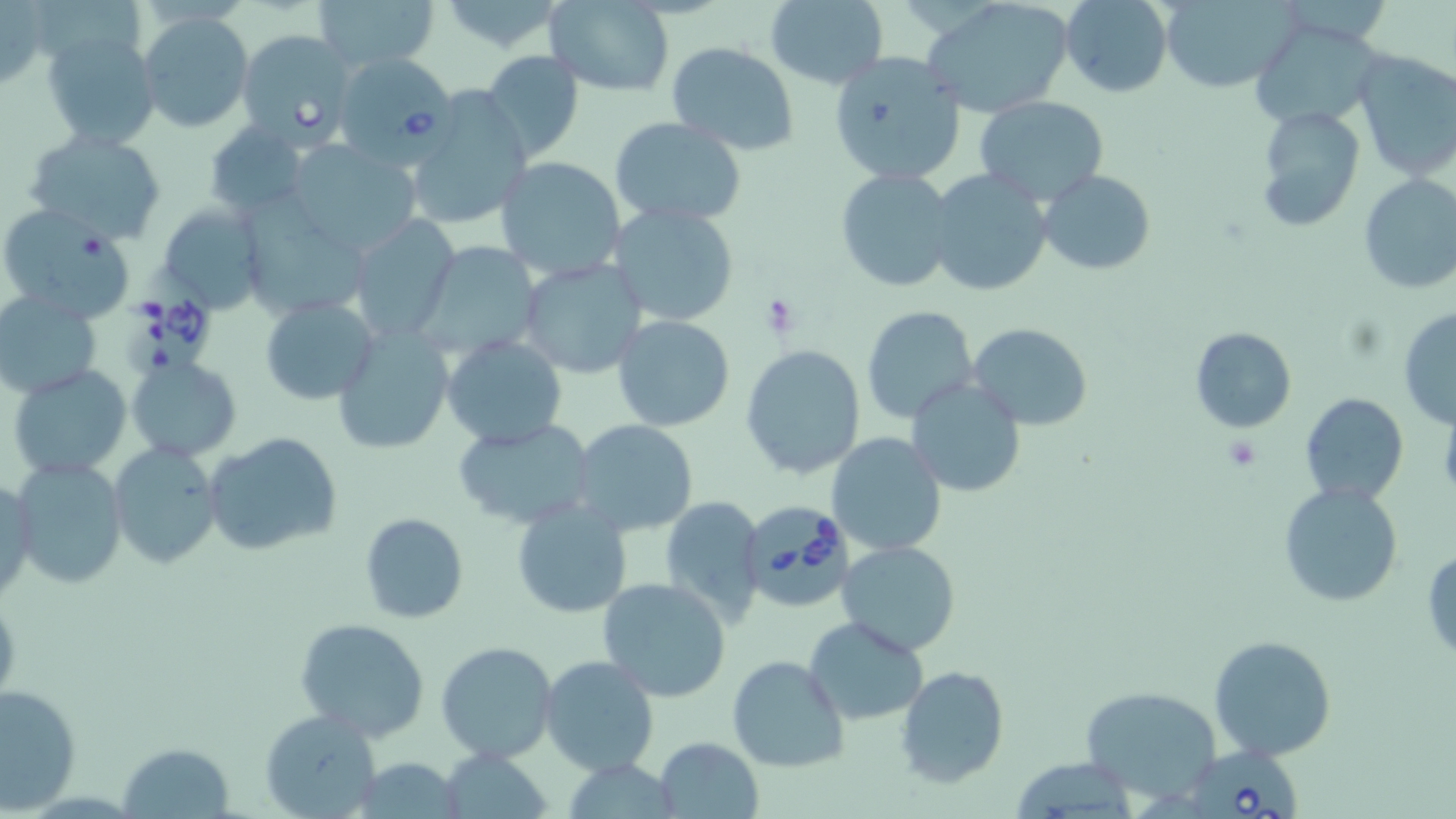
Summary:
  - Coordinate format: approximate bounding boxes as [x1, y1, x2, y2] in pixels
  - Uninfected red blood cell locations: [315, 0, 439, 74], [764, 0, 887, 89], [923, 0, 1077, 120], [1060, 0, 1172, 97], [1161, 0, 1295, 93], [0, 2, 50, 90], [432, 2, 572, 53], [543, 2, 676, 96], [137, 11, 253, 133], [1254, 22, 1391, 129], [41, 29, 161, 150], [235, 29, 357, 153], [666, 42, 800, 154], [479, 49, 586, 163], [1349, 49, 1456, 183], [828, 51, 966, 187], [405, 91, 534, 230], [975, 95, 1108, 206], [1254, 104, 1366, 233], [609, 118, 745, 227], [204, 123, 310, 218], [22, 129, 170, 242], [287, 143, 420, 256], [495, 157, 628, 280], [835, 168, 957, 293], [927, 169, 1052, 298], [1038, 170, 1156, 274], [1357, 174, 1456, 296], [245, 187, 365, 320], [156, 203, 264, 313], [608, 203, 739, 327], [0, 204, 137, 324], [346, 217, 463, 344], [430, 245, 552, 354], [518, 258, 648, 379], [1, 292, 102, 400], [260, 297, 379, 404], [861, 304, 979, 424], [1397, 307, 1456, 429], [611, 314, 735, 431], [968, 323, 1093, 429], [1189, 326, 1297, 433], [331, 327, 452, 456], [441, 335, 568, 450], [740, 344, 867, 479], [128, 356, 241, 461], [8, 364, 132, 480], [906, 377, 1028, 497], [1300, 393, 1409, 506], [454, 418, 598, 529], [571, 419, 700, 537], [204, 430, 342, 555], [827, 432, 946, 558], [109, 443, 225, 569], [11, 459, 127, 591], [1, 474, 38, 603], [1277, 481, 1404, 608], [658, 495, 767, 625], [512, 499, 633, 619], [359, 512, 469, 624], [835, 540, 961, 656], [1423, 545, 1456, 661], [596, 577, 733, 702], [294, 618, 431, 741], [804, 618, 928, 725], [1207, 634, 1337, 762], [436, 640, 558, 762], [539, 654, 660, 777], [726, 654, 849, 774], [896, 664, 1009, 787], [2, 684, 80, 811], [1080, 685, 1224, 803], [259, 709, 381, 819], [654, 736, 763, 817], [117, 742, 234, 817], [442, 746, 550, 818], [349, 758, 470, 817]
  - Babesia divergens-infected red blood cell locations: [329, 51, 456, 166], [121, 265, 220, 377], [743, 497, 852, 606], [1189, 738, 1306, 819]
  - Platelet locations: [761, 294, 803, 336], [1221, 435, 1263, 473]
  - Slide-level diagnosis: Babesia divergens
  - Field of view: single
  - Magnification: 1000x
  - Modality: optical microscopy
  - Stain: May-Grünwald-Giemsa
  - Image size: 1456×819 pixels
  - Preparation: thin blood smear